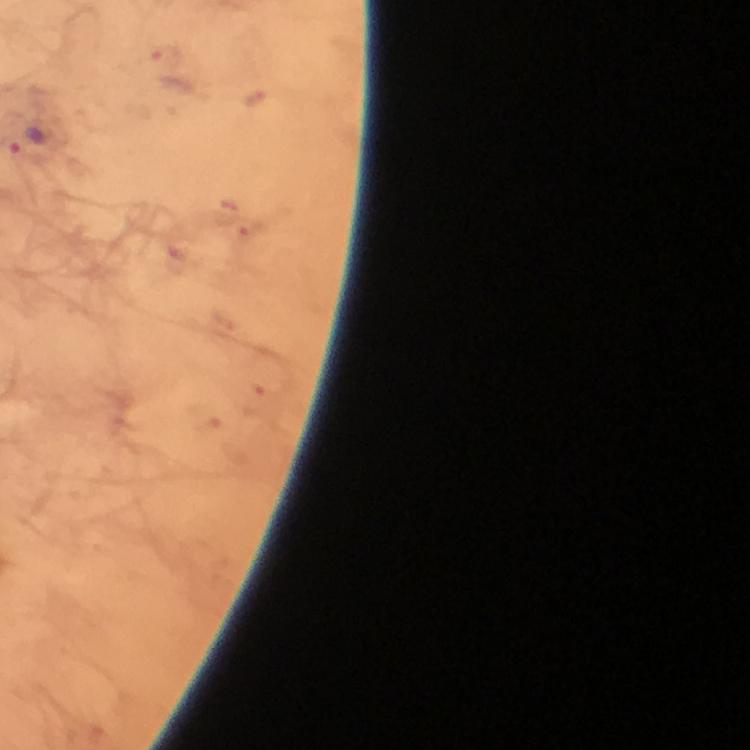

cropped from = one field of view
preparation = thick blood film
immersion oil = applied
image size = 750×750 pixels
Plasmodium parasite locations = approximate object centers, in pixels from the top-left corner: (x=25, y=142)
magnification = 100x
stain = Giemsa
capture = smartphone mounted on the microscope
context = from a diagnostic examination for malaria